Classify this cell by malaria status.
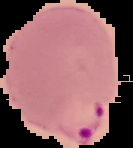

It is parasitized.

The area outside the segmented cell region is set to black. Image is 133×148 pixels. From a thin blood film.